Identify the parasite.
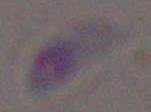

This is Toxoplasma gondii.

{
  "magnification": "1000x",
  "modality": "micrograph"
}